Point out each malaria parasite.
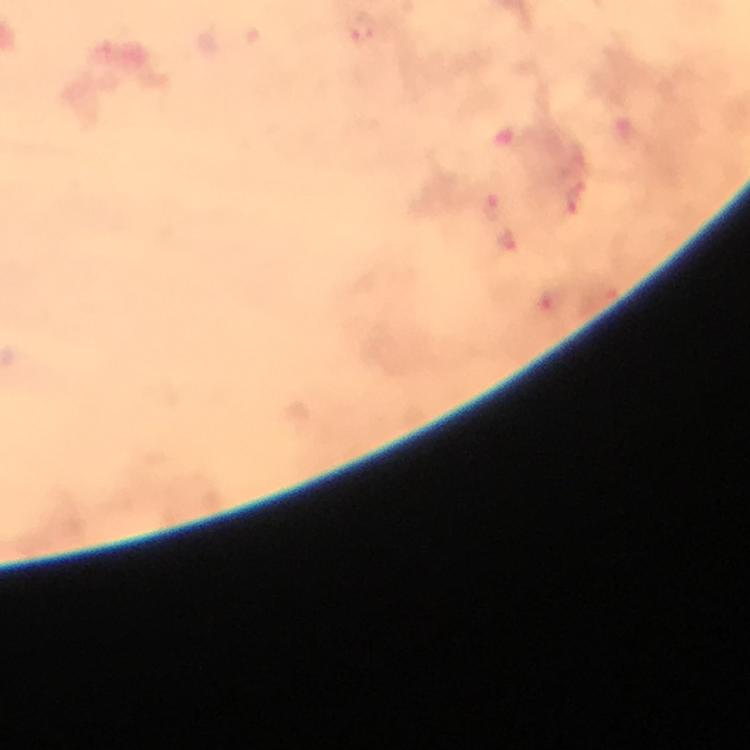

Approximate centers as (x, y) in pixels.
Malaria parasites: (363, 30), (575, 199), (494, 207).

A crop from one field of view. Giemsa stain. Immersion oil was used. Image is 750×750 pixels. From a malaria diagnostic workup. 100x magnification. Photographed through the microscope with a smartphone camera. Thick blood film.